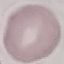

Summary:
  - Result: negative for malaria parasites
  - Stain: Giemsa
  - Image type: automatically extracted cell patch, resized to 64 × 64 pixels
  - Preparation: thin blood smear
  - Capture: smartphone camera at the microscope eyepiece